Assess this cell for malaria.
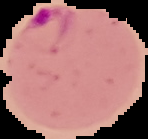
It is parasitized.

image size = 148×139 pixels
preparation = thin blood film
image type = segmented cell region with the area outside set to black